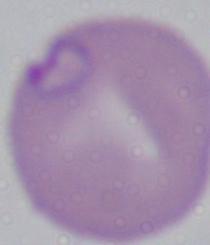
Micrograph. Captured at 1000x magnification. A Babesia parasite is shown.